Assess the morphology of the erythrocytes.
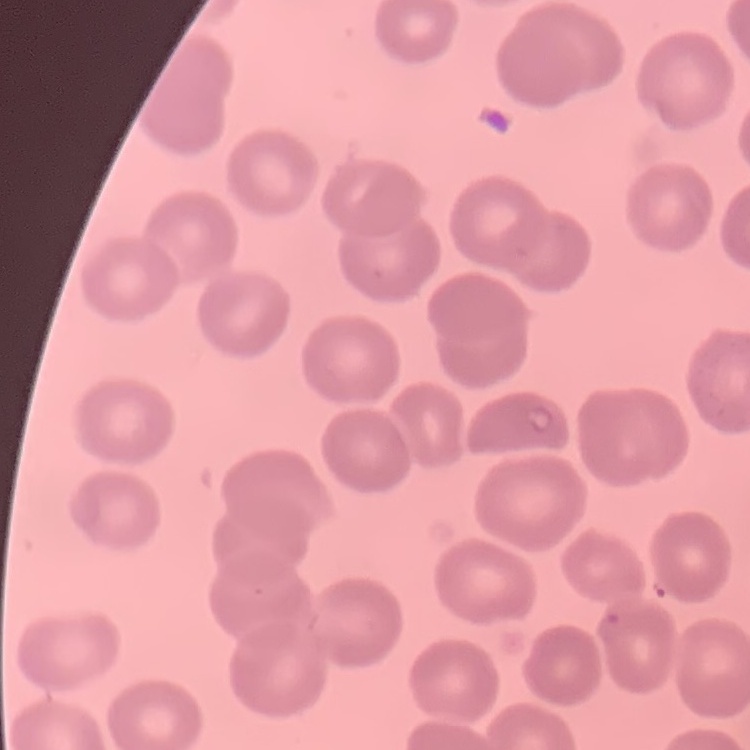
They show no rouleaux formation.

preparation: thin blood film
image_type: square crop of a larger photomicrograph
stain: Field's or Giemsa